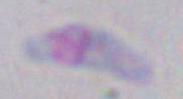
Summary:
  - Magnification: 1000x
  - Identification: Toxoplasma gondii
  - Modality: photomicrograph